Classify this cell by malaria status.
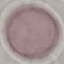

Uninfected.

Cell patch, automatically extracted from a larger field of view and resized to 64 × 64 pixels. Acquired by smartphone through the microscope eyepiece. Giemsa stain. Thin smear of blood.